Comment on the morphology of the erythrocytes.
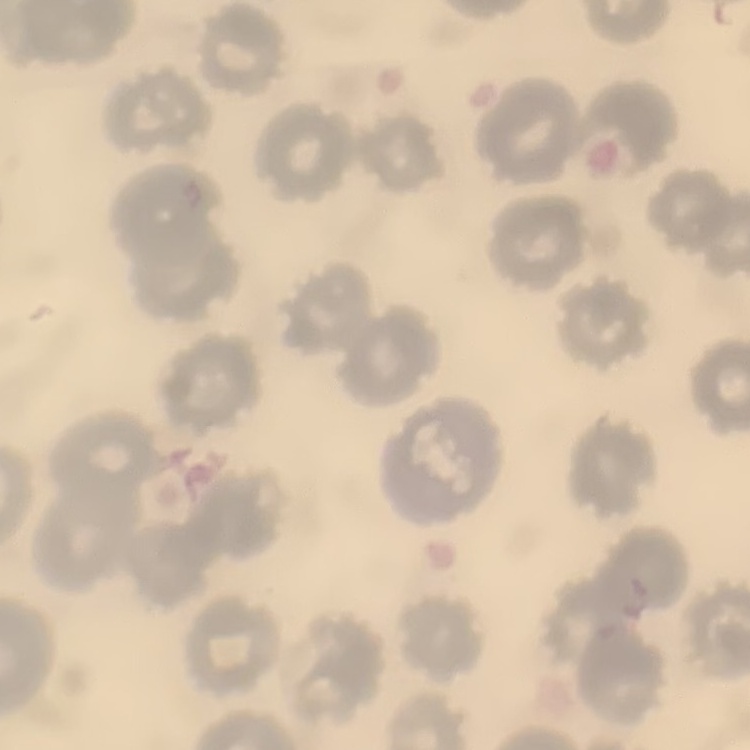

They show no rouleaux formation.

Square crop of a larger photomicrograph. Stained with either Field's or Giemsa. Thin blood smear.